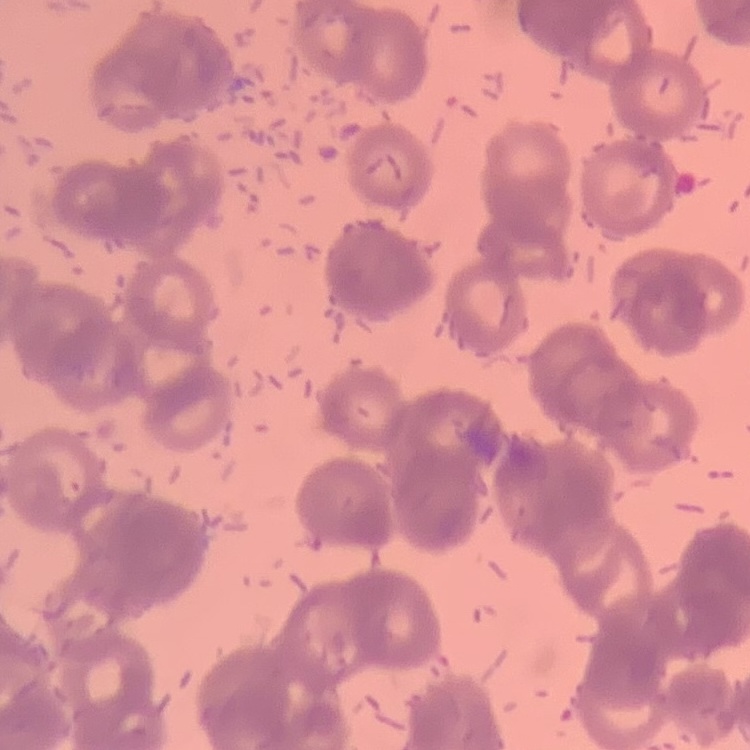 The red blood cells exhibit rouleaux formation. Field's or Giemsa stain. One tile cut from a larger photomicrograph. Thin blood film.